Assess this cell for malaria.
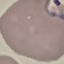
It is parasitized.

Summary:
  - Capture: smartphone camera at the microscope eyepiece
  - Image type: cell patch, automatically extracted from a larger field of view and resized to 64 × 64 pixels
  - Stain: Giemsa
  - Preparation: thin blood smear